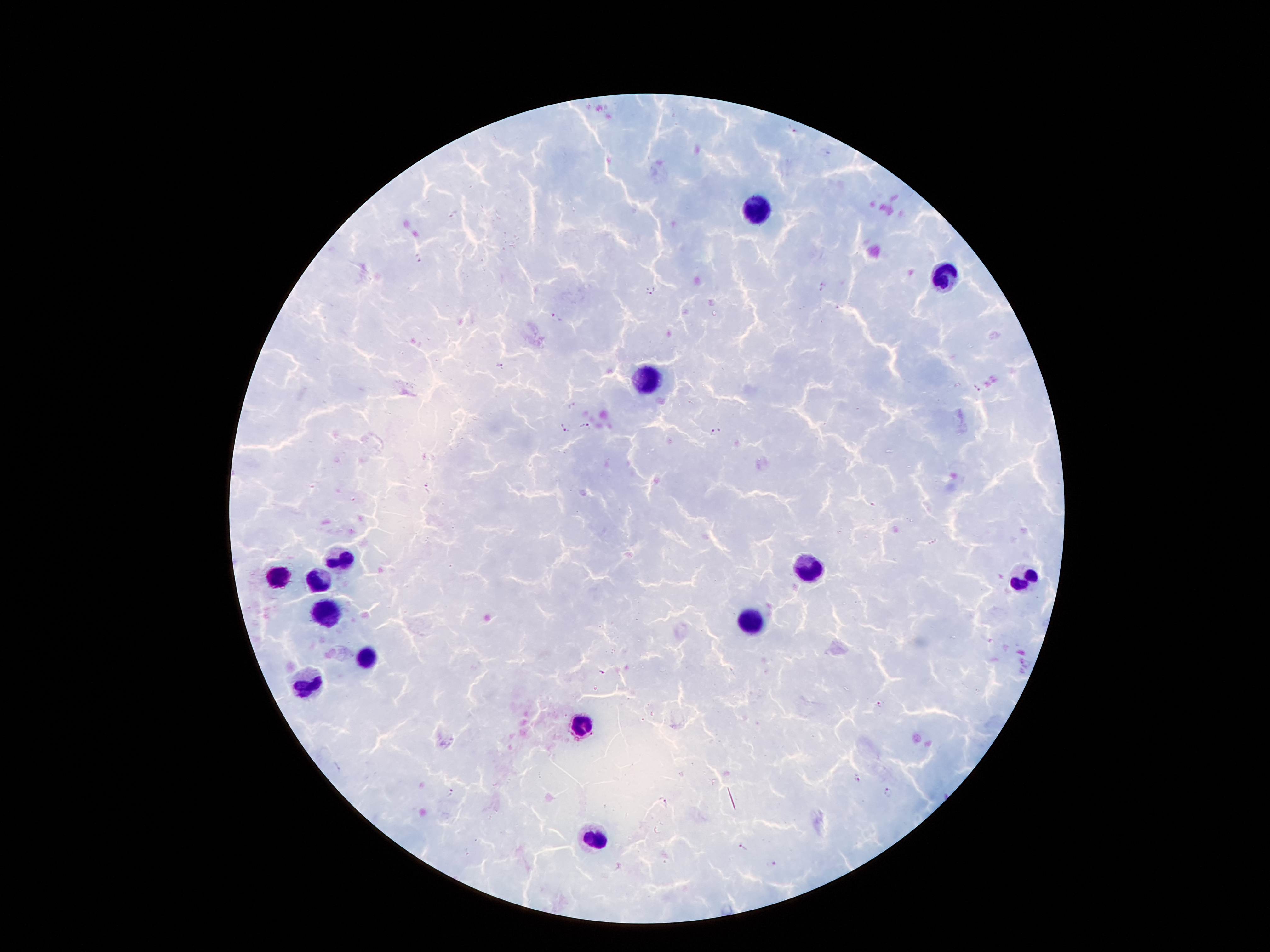

Approximate object centers, in pixels from the top-left corner. Plasmodium parasite locations: (x=793, y=129), (x=419, y=260), (x=822, y=289), (x=651, y=290), (x=556, y=318), (x=499, y=365), (x=976, y=388), (x=586, y=425), (x=566, y=427), (x=715, y=431), (x=426, y=488), (x=603, y=673), (x=879, y=704), (x=856, y=778), (x=451, y=792), (x=888, y=793), (x=664, y=802), (x=742, y=847). Leukocyte locations: (x=756, y=208), (x=945, y=276), (x=643, y=378), (x=342, y=561), (x=808, y=569), (x=277, y=578), (x=1027, y=578), (x=315, y=580), (x=321, y=611), (x=750, y=620), (x=365, y=656), (x=307, y=681), (x=582, y=723), (x=594, y=840). One field from this slide. Image is 1270×952 pixels. 100x magnification. Patient malaria status: positive for Plasmodium falciparum. Thick blood film. Smartphone photograph taken through the microscope eyepiece. Giemsa-stained preparation.